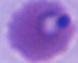
{
  "modality": "micrograph",
  "identification": "Plasmodium",
  "magnification": "400x or 1000x"
}